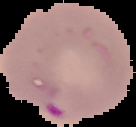
Summary:
  - Image size: 136×127 pixels
  - Preparation: thin blood smear
  - Malaria status: parasitized
  - Image type: cell region segmented out of the field of view; surrounding area masked to black